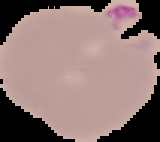
Summary:
  - Image size: 160×142 pixels
  - Malaria status: parasitized
  - Image type: segmented cell region on a black background
  - Preparation: thin blood film